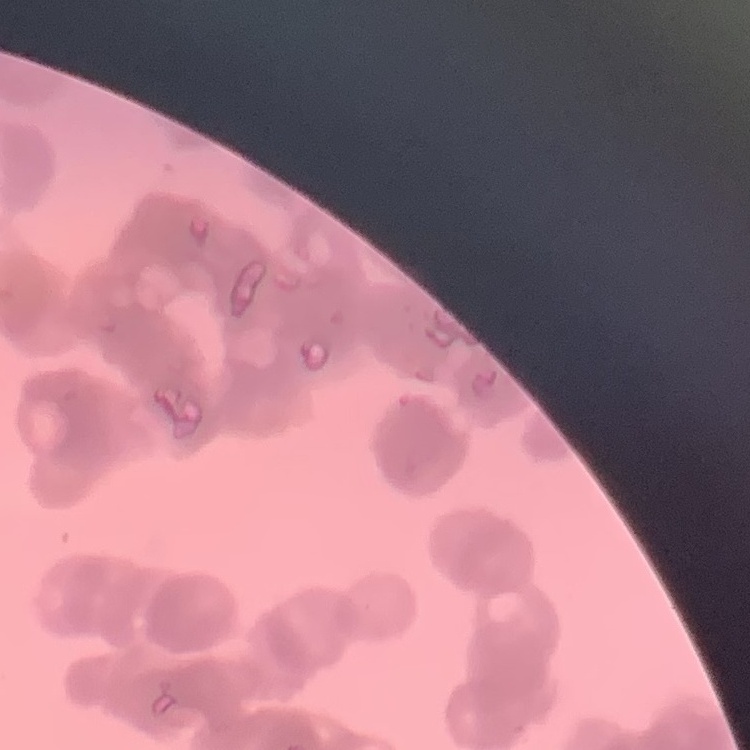
erythrocyte morphology = rouleaux formation
image type = square crop of a larger photomicrograph
stain = Field's or Giemsa
preparation = thin blood film